Identify the cell.
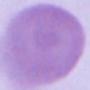

An erythrocyte.

1000x magnification. Micrograph.